State which parasite is depicted.
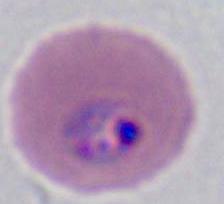

This is Plasmodium.

Photomicrograph. 400x or 1000x magnification.